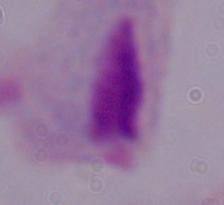
modality = photomicrograph
identification = trichomonad
magnification = 1000x